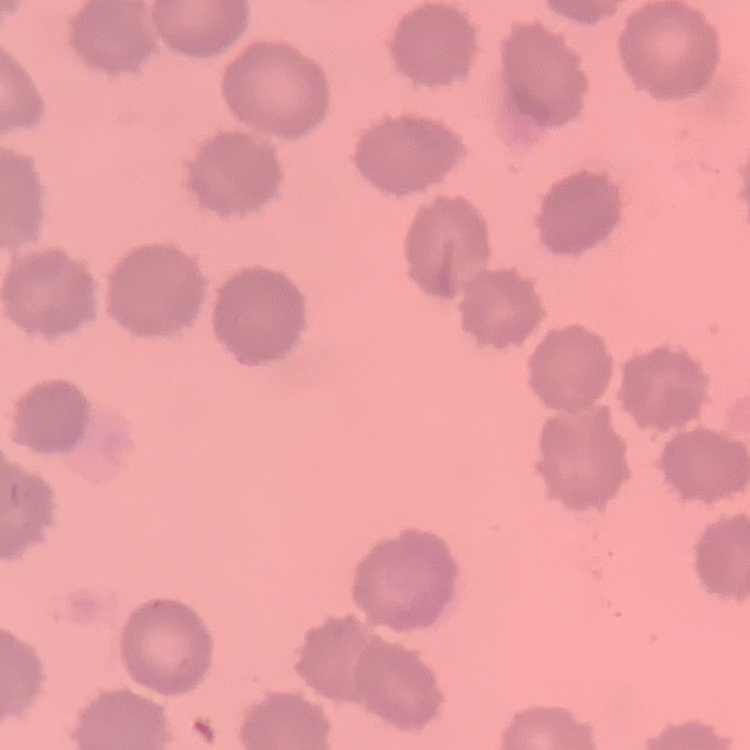
Summary:
  - Red blood cell morphology: no rouleaux formation
  - Stain: Field's or Giemsa
  - Preparation: thin blood film
  - Image type: one tile cut from a larger photomicrograph